Outline each blood parasite and name the species.
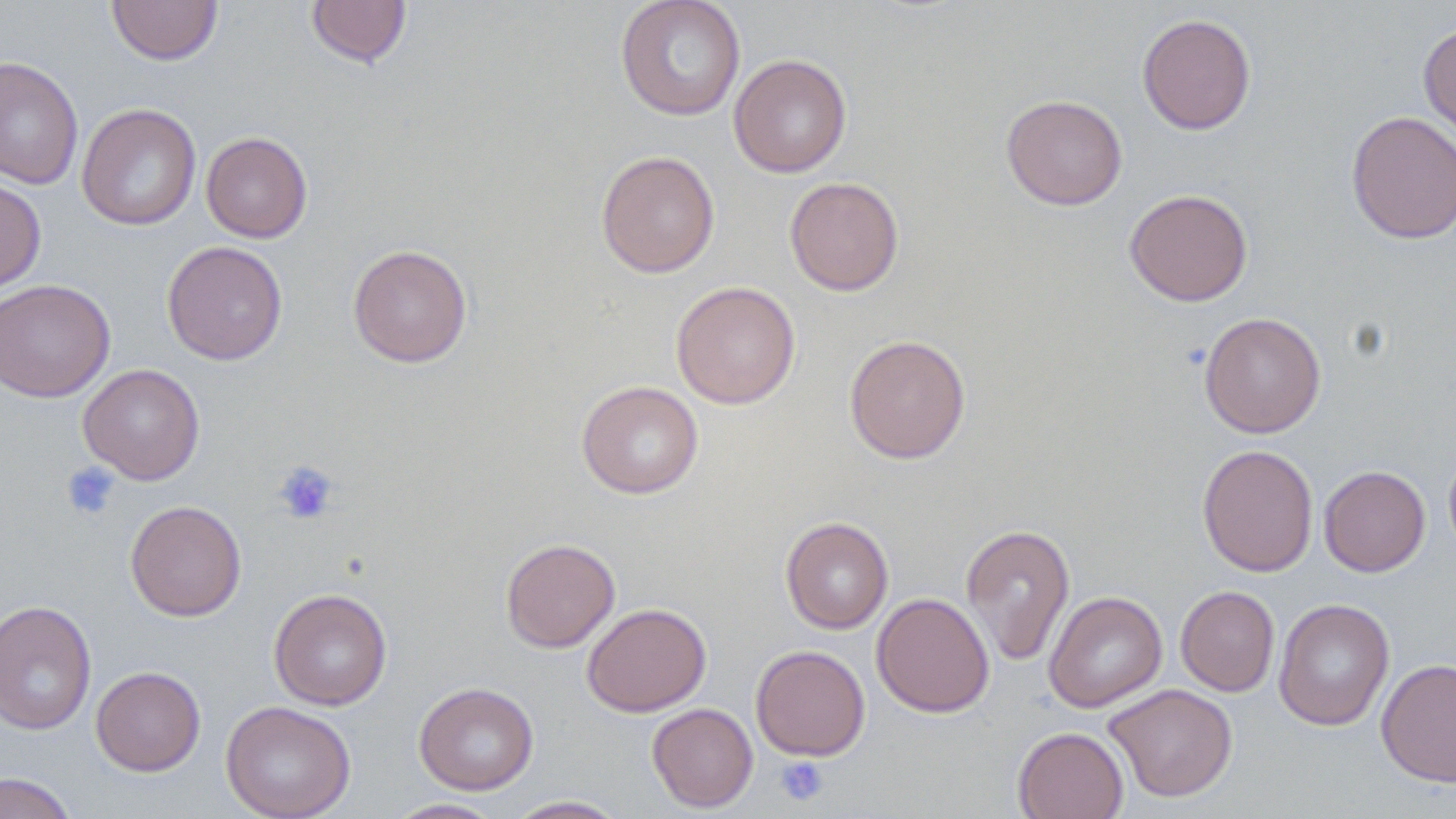

No blood parasites observed.

Summary:
  - Coordinate format: approximate bounding boxes as [x1, y1, x2, y2] in pixels
  - Uninfected red blood cell locations: [106, 0, 223, 66], [305, 0, 412, 69], [614, 0, 747, 121], [1137, 13, 1256, 135], [1418, 22, 1456, 149], [729, 53, 852, 178], [0, 56, 84, 191], [1001, 94, 1127, 210], [77, 103, 201, 231], [1345, 110, 1456, 245], [201, 132, 313, 243], [596, 150, 720, 278], [0, 177, 46, 294], [784, 177, 904, 296], [1124, 188, 1253, 306], [162, 241, 288, 365], [347, 244, 473, 368], [0, 279, 115, 402], [670, 281, 801, 409], [1199, 312, 1326, 438], [844, 334, 971, 464], [78, 363, 205, 485], [576, 380, 704, 499], [1197, 444, 1319, 577], [1443, 444, 1456, 562], [1318, 465, 1430, 577], [125, 500, 247, 621], [780, 516, 894, 634], [960, 523, 1075, 665], [500, 538, 620, 653], [1176, 585, 1279, 697], [268, 588, 392, 710], [1043, 591, 1167, 713], [871, 593, 995, 718], [1273, 598, 1395, 732], [0, 600, 97, 735], [582, 602, 711, 717], [750, 645, 870, 761], [1376, 657, 1456, 788], [90, 666, 206, 776], [414, 681, 539, 795], [1104, 683, 1238, 802], [220, 700, 356, 819], [647, 703, 758, 812], [1012, 726, 1129, 819], [0, 772, 78, 819], [505, 795, 629, 818], [384, 798, 506, 818]
  - Platelet locations: [272, 460, 339, 525], [61, 461, 121, 521], [774, 755, 829, 807]
  - Slide-level diagnosis: no evidence of blood parasites
  - Stain: May-Grünwald-Giemsa
  - Field of view: single
  - Magnification: 1000x
  - Preparation: thin blood film
  - Modality: light microscopy
  - Image size: 1456×819 pixels